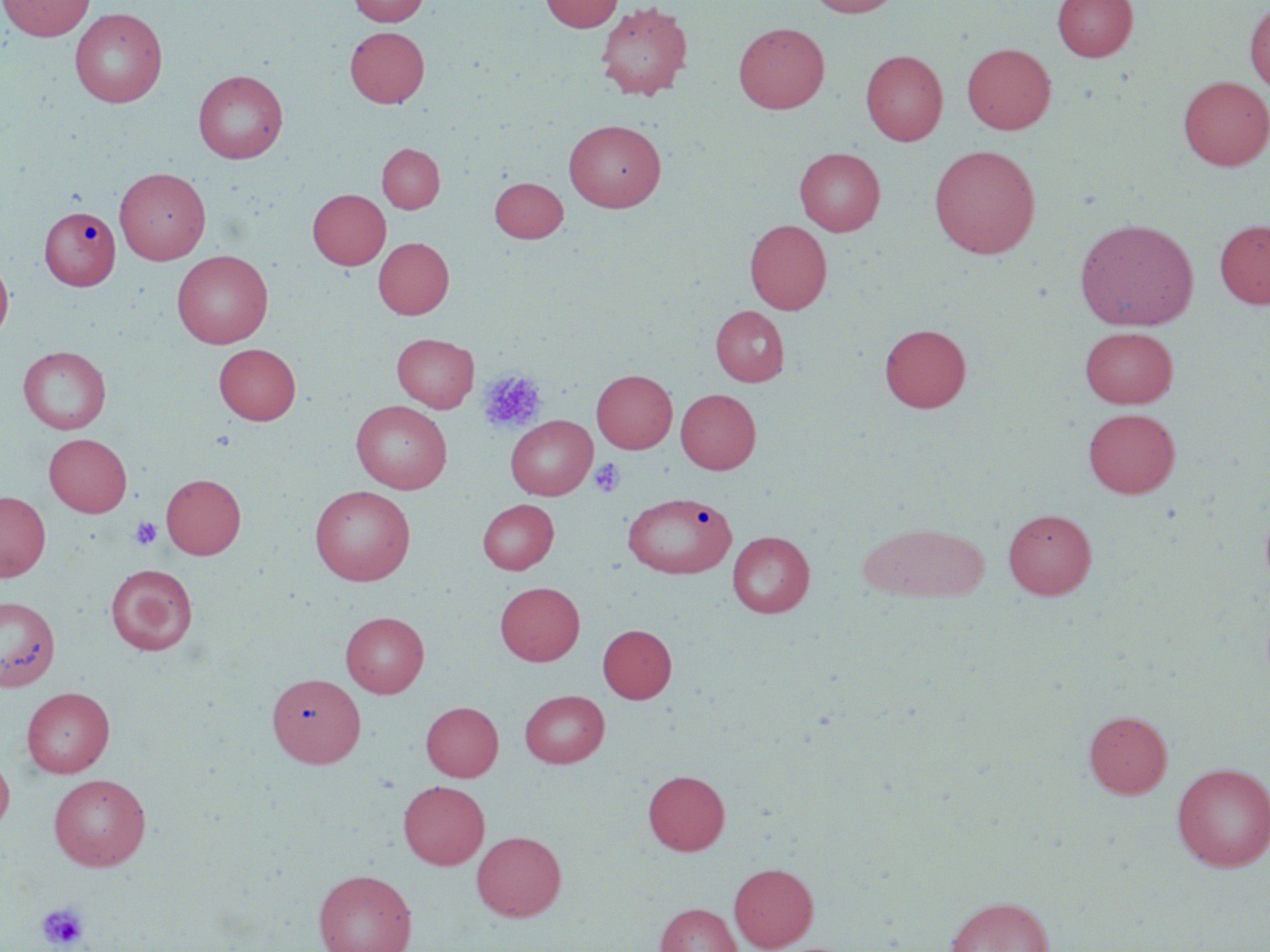 Approximate bounding boxes as [x1, y1, x2, y2] in pixels. Platelet locations: [477, 370, 546, 433], [590, 458, 625, 498], [129, 517, 162, 550], [37, 901, 90, 950]. Uninfected red blood cell locations: [0, 0, 94, 40], [347, 0, 429, 26], [540, 0, 622, 32], [806, 0, 903, 17], [1052, 0, 1138, 61], [595, 1, 693, 101], [1244, 2, 1270, 93], [69, 8, 167, 107], [733, 23, 830, 113], [345, 26, 429, 107], [962, 43, 1056, 134], [861, 50, 948, 145], [193, 69, 288, 163], [1178, 76, 1270, 170], [563, 119, 667, 212], [377, 143, 444, 212], [929, 144, 1041, 258], [795, 147, 885, 235], [115, 167, 211, 264], [489, 177, 568, 242], [308, 189, 390, 269], [39, 205, 121, 290], [1075, 217, 1199, 330], [1215, 218, 1270, 309], [745, 220, 832, 314], [373, 237, 453, 318], [172, 250, 273, 348], [0, 255, 14, 345], [711, 305, 789, 385], [879, 323, 972, 413], [1080, 326, 1178, 408], [391, 332, 479, 412], [214, 343, 301, 424], [18, 346, 111, 433], [593, 369, 677, 453], [676, 389, 761, 473], [352, 400, 452, 494], [1083, 407, 1180, 498], [506, 415, 597, 500], [44, 433, 132, 516], [161, 473, 245, 559], [309, 485, 415, 585], [0, 490, 50, 581], [622, 492, 735, 578], [1259, 497, 1270, 593], [478, 499, 558, 574], [1003, 508, 1096, 598], [859, 521, 989, 602], [727, 531, 814, 618], [105, 563, 198, 655], [495, 581, 584, 665], [0, 596, 60, 692], [341, 611, 429, 697], [598, 624, 676, 703], [267, 673, 365, 767], [21, 687, 115, 777], [520, 689, 610, 767], [421, 701, 503, 780], [1083, 710, 1172, 798], [0, 749, 14, 835], [1171, 762, 1270, 872], [643, 770, 730, 855], [49, 773, 151, 870], [399, 780, 489, 868], [472, 830, 566, 921], [729, 862, 818, 951], [313, 868, 417, 952], [944, 895, 1054, 952], [655, 903, 741, 952]. Slide-level diagnosis: negative for blood parasites. 1000x magnification. May-Grünwald-Giemsa-stained preparation. Optical microscopy. One field of a larger specimen. Image is 1270×952 pixels. Thin blood smear.